Classify this cell by malaria status.
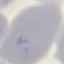
Uninfected.

image type = cell patch, automatically extracted from a larger field of view and resized to 64 × 64 pixels
capture = smartphone camera at the microscope eyepiece
stain = Giemsa
preparation = thin blood film